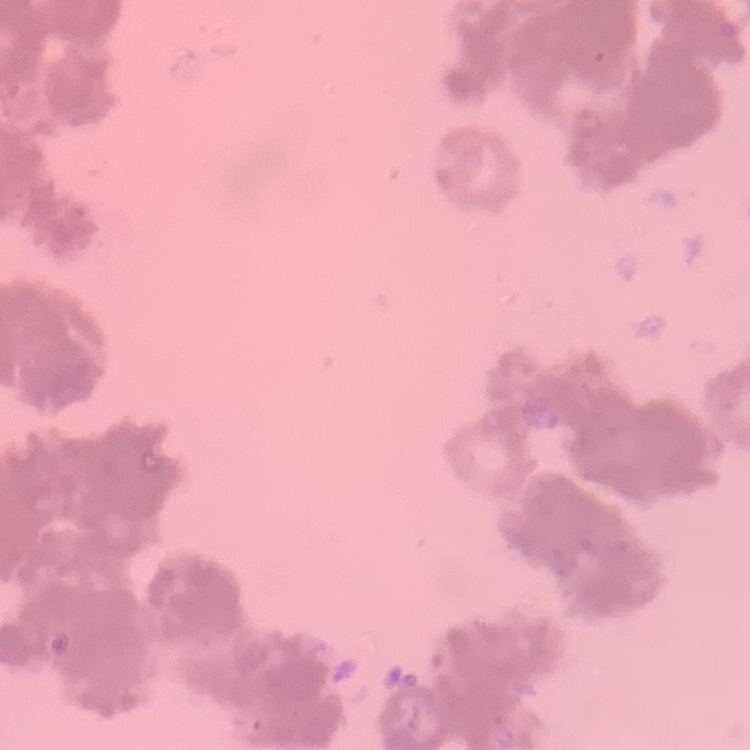
{
  "red_blood_cell_morphology": "rouleaux formation",
  "preparation": "thin blood smear",
  "image_type": "square crop of a larger photomicrograph",
  "stain": "Field's or Giemsa"
}